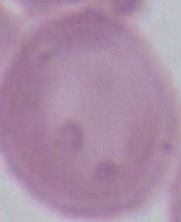

Summary:
  - Modality: micrograph
  - Magnification: 1000x
  - Identification: erythrocyte